Give the preparation type.
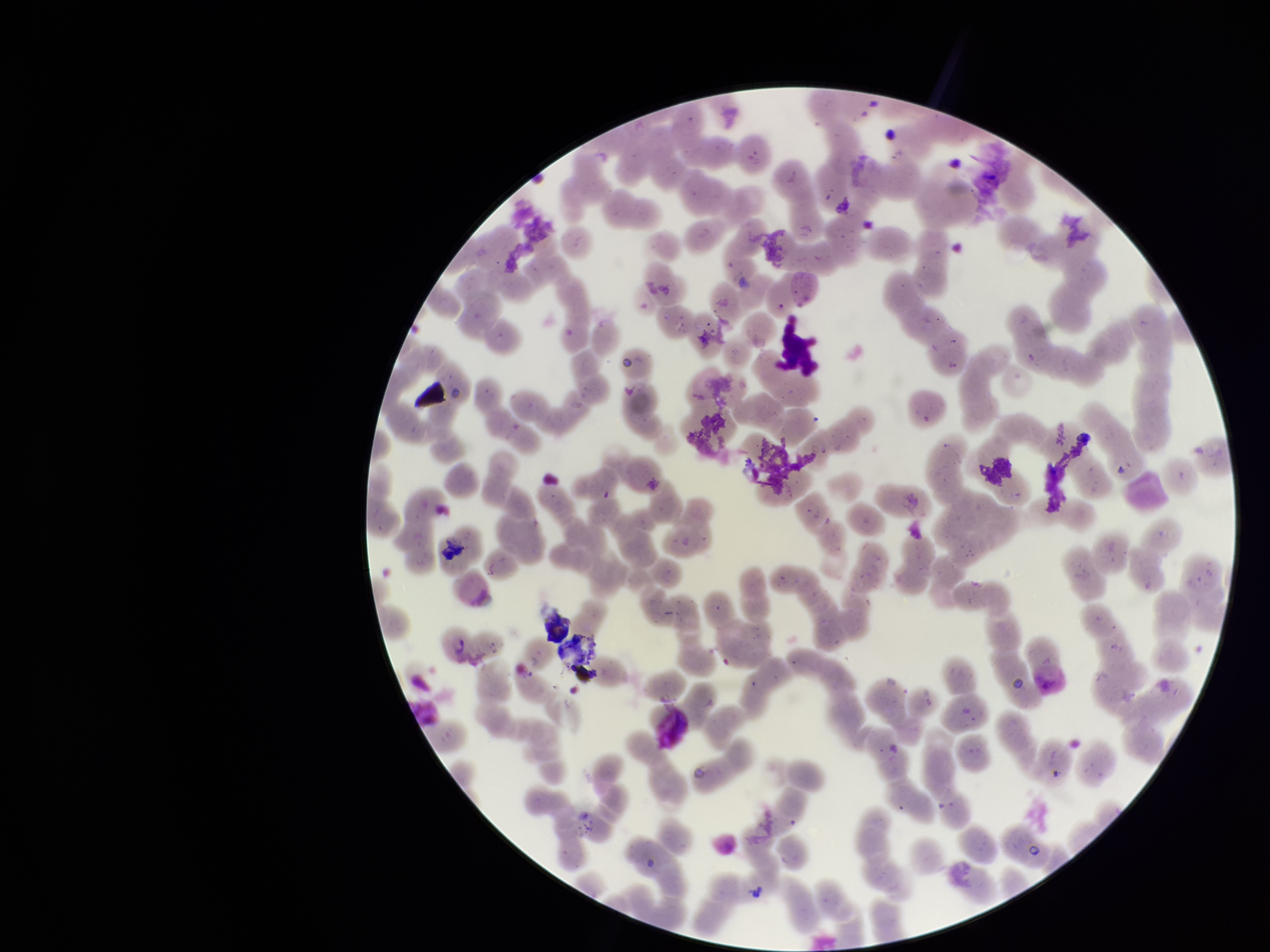

A thin smear.

Summary:
  - Stain: Giemsa
  - Field of view: one from this slide
  - Capture: smartphone photograph through the microscope eyepiece
  - Patient malaria status: positive
  - Red blood cell count: 240
  - Image size: 1270×952 pixels
  - Parasitized red blood cells: none seen
  - Species reported for this patient: Plasmodium vivax
  - Parasitized red blood cell count: 0